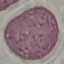 Malaria status: uninfected. Acquired by smartphone through the microscope eyepiece. Giemsa stain. Cell patch, automatically extracted from a larger field of view and resized to 64 × 64 pixels. Thin smear of blood.